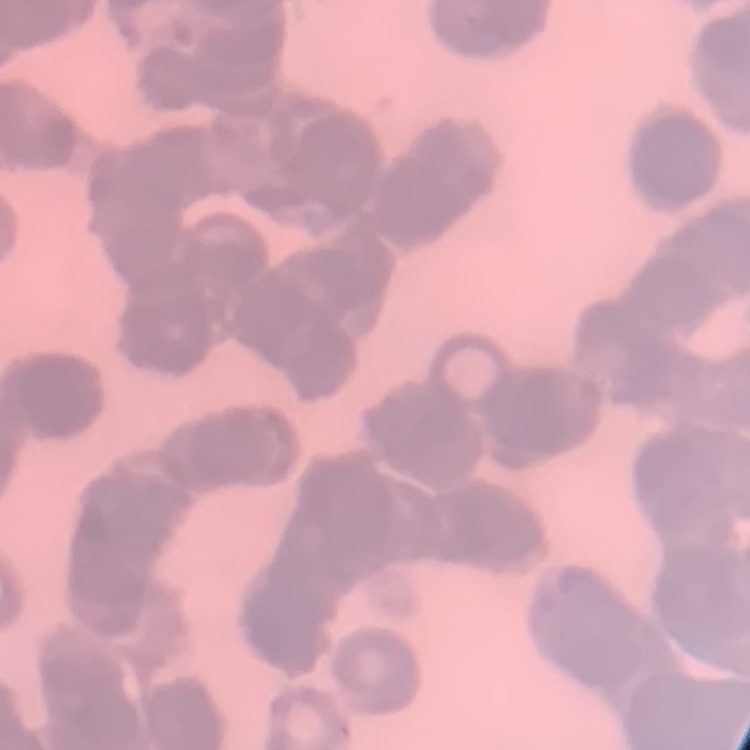

Summary:
  - Erythrocyte morphology: rouleaux formation
  - Image type: one tile cut from a larger photomicrograph
  - Stain: Field's or Giemsa
  - Preparation: thin peripheral smear